Point out each malaria parasite.
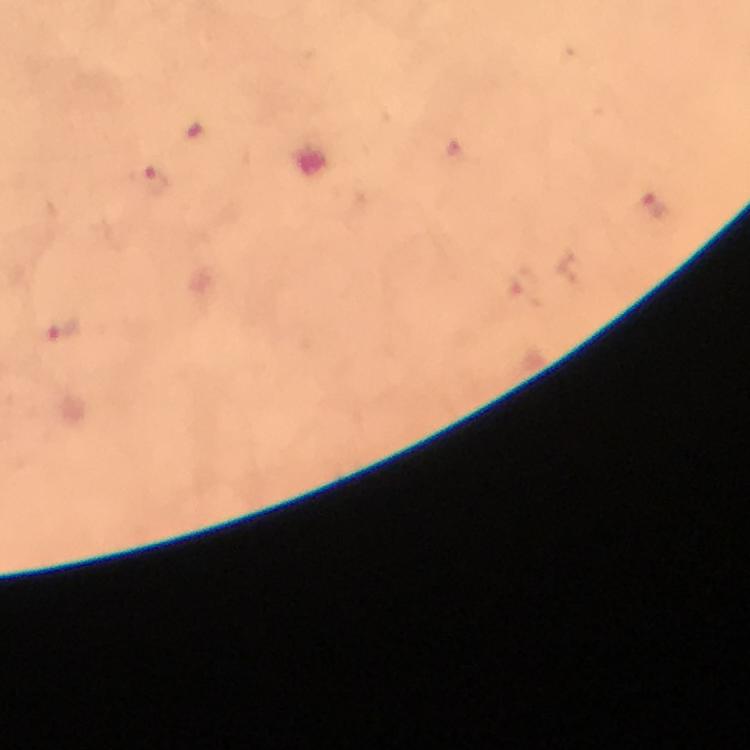
Approximate centers as [x, y] in pixels.
Malaria parasites: [154, 184], [66, 330].

magnification = 100x
stain = Giemsa
cropped from = a single field of view
image size = 750×750 pixels
immersion oil = applied
capture = smartphone camera through the microscope
preparation = thick blood film
context = from a diagnostic examination for malaria